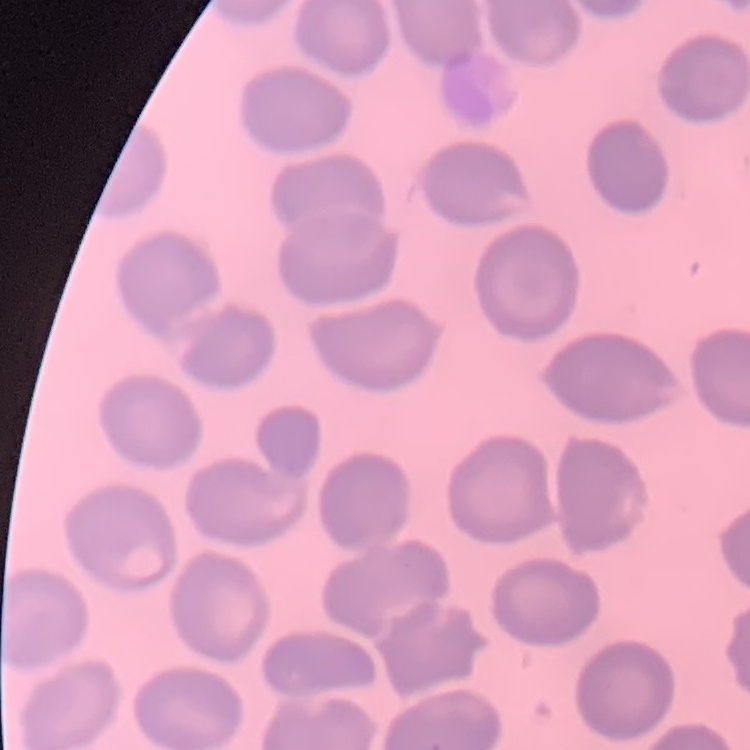

Summary:
  - Erythrocyte morphology: no rouleaux formation
  - Preparation: thin blood smear
  - Image type: one tile cut from a larger photomicrograph
  - Stain: Field's or Giemsa